Identify the parasite.
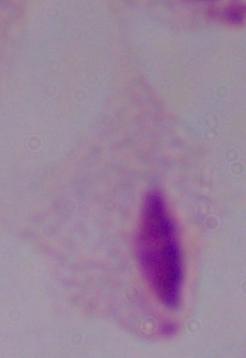

This is a trichomonad.

Captured at 1000x magnification. Photomicrograph.